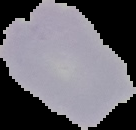

Summary:
  - Image type: segmented cell region on a black background
  - Result: no Plasmodium parasites seen
  - Preparation: thin blood smear
  - Image size: 136×130 pixels